Comment on the morphology of the red blood cells.
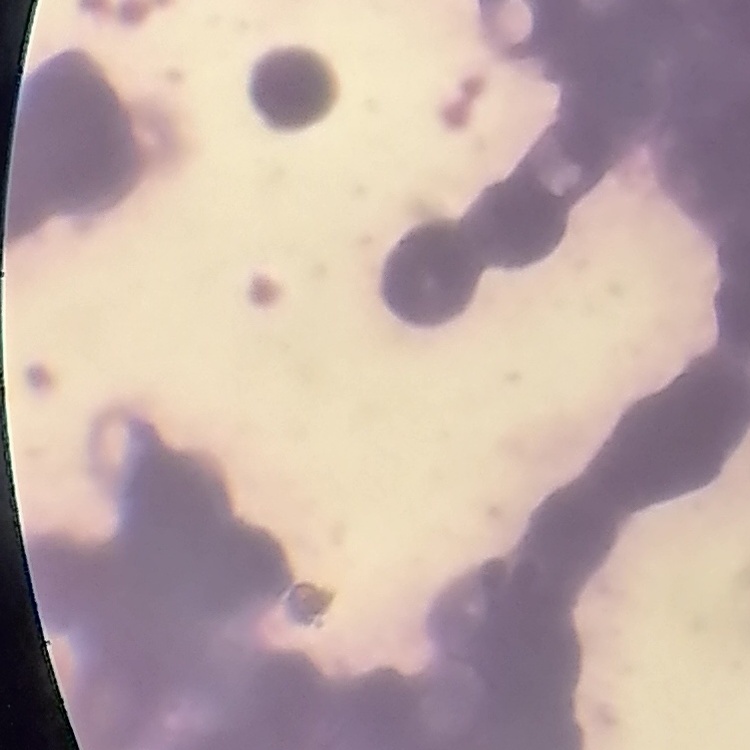
Rouleaux formation.

image type = square crop of a larger photomicrograph
stain = Field's or Giemsa
preparation = thin blood smear